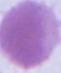

{
  "modality": "photomicrograph",
  "magnification": "1000x",
  "identification": "red blood cell"
}